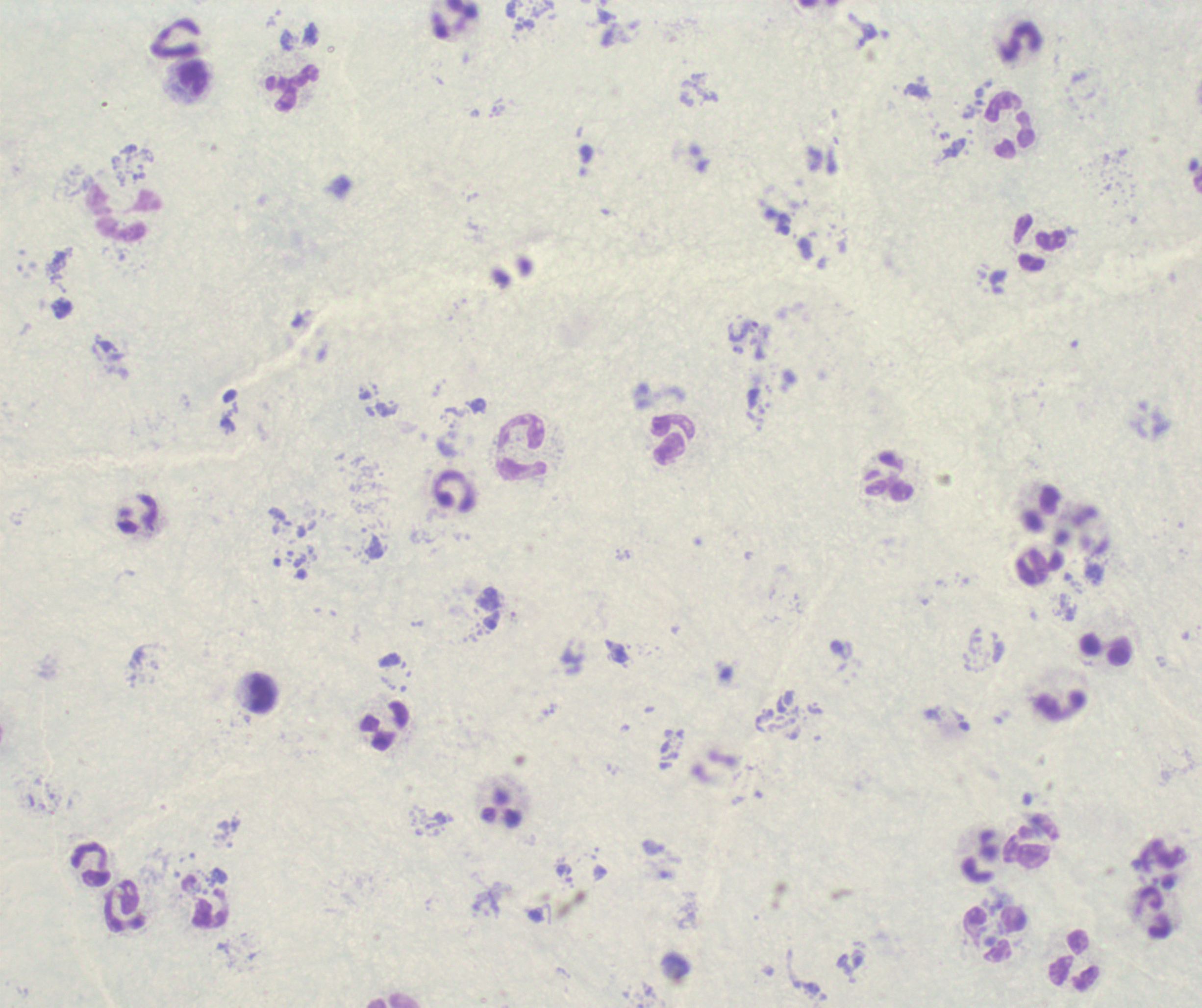

Approximate object centers, in pixels from the top-left corner.
Summary:
  - Trophozoite locations: (x=743, y=332)
  - Leukocyte locations: (x=1021, y=43), (x=193, y=78), (x=292, y=88), (x=1011, y=126), (x=124, y=211), (x=1040, y=243), (x=673, y=441), (x=521, y=447), (x=889, y=475), (x=455, y=492), (x=1040, y=566), (x=1106, y=649), (x=263, y=693), (x=385, y=727), (x=1031, y=840), (x=91, y=866), (x=124, y=907), (x=1153, y=913), (x=994, y=934), (x=1075, y=960)
  - Image size: 1202×1008 pixels
  - Field of view: single
  - Context: previously used in a real diagnosis
  - Preparation: thick blood smear
  - Stain: Romanowsky
  - Result: positive for Plasmodium parasites
  - Background quality: unsatisfactory
  - Magnification: 100x